State which parasite is depicted.
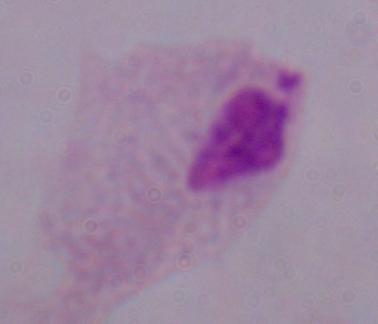
A trichomonad.

1000x magnification. Micrograph.